State which cell type is depicted.
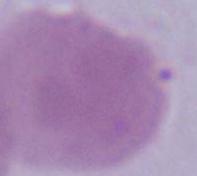
An erythrocyte.

{
  "modality": "micrograph",
  "magnification": "1000x"
}